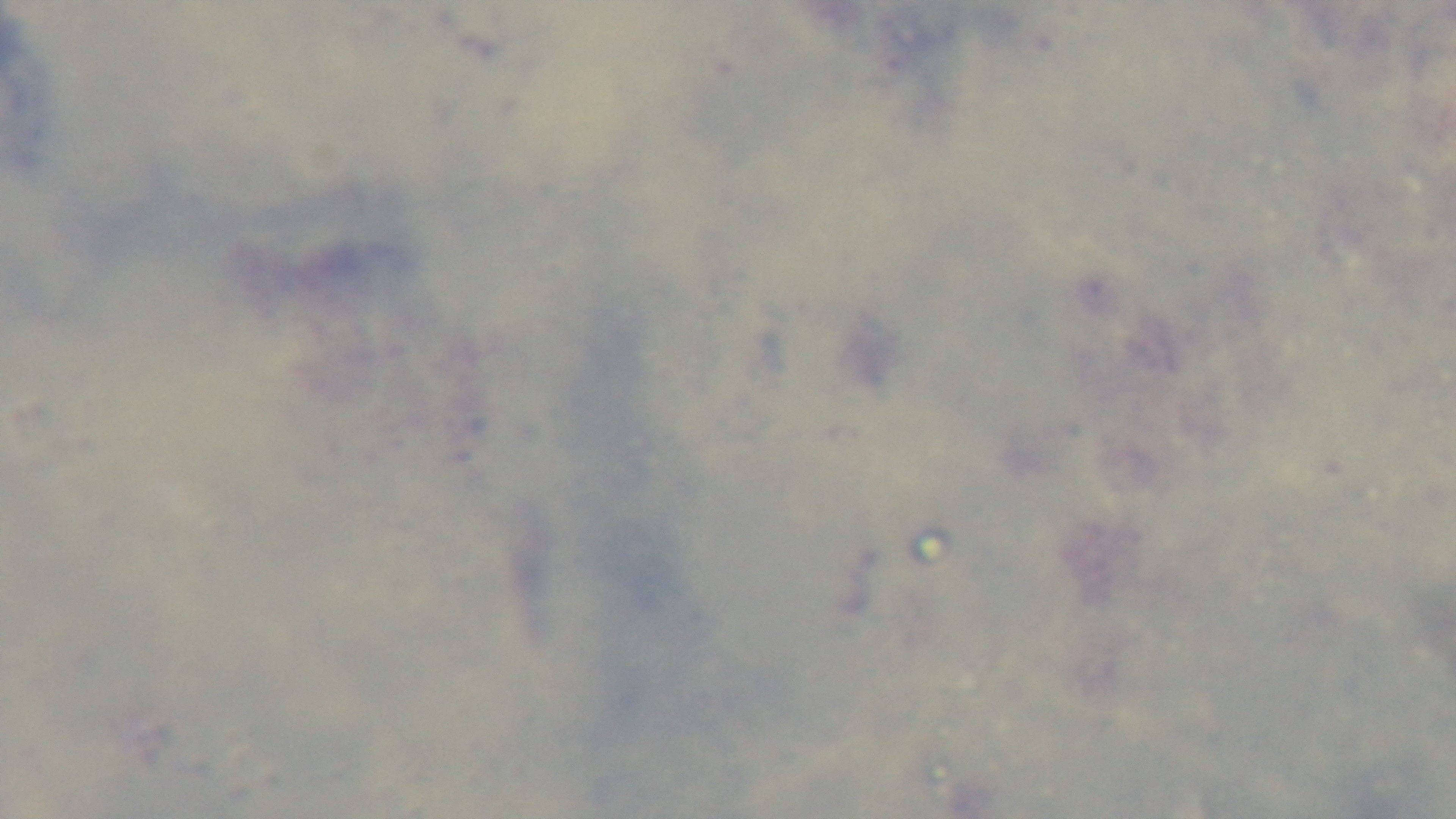
malaria status = negative
modality = light microscopy
objective = 100x oil immersion
field of view = single
capture = mounted 4K digital camera
preparation = thick blood film
stain = Giemsa